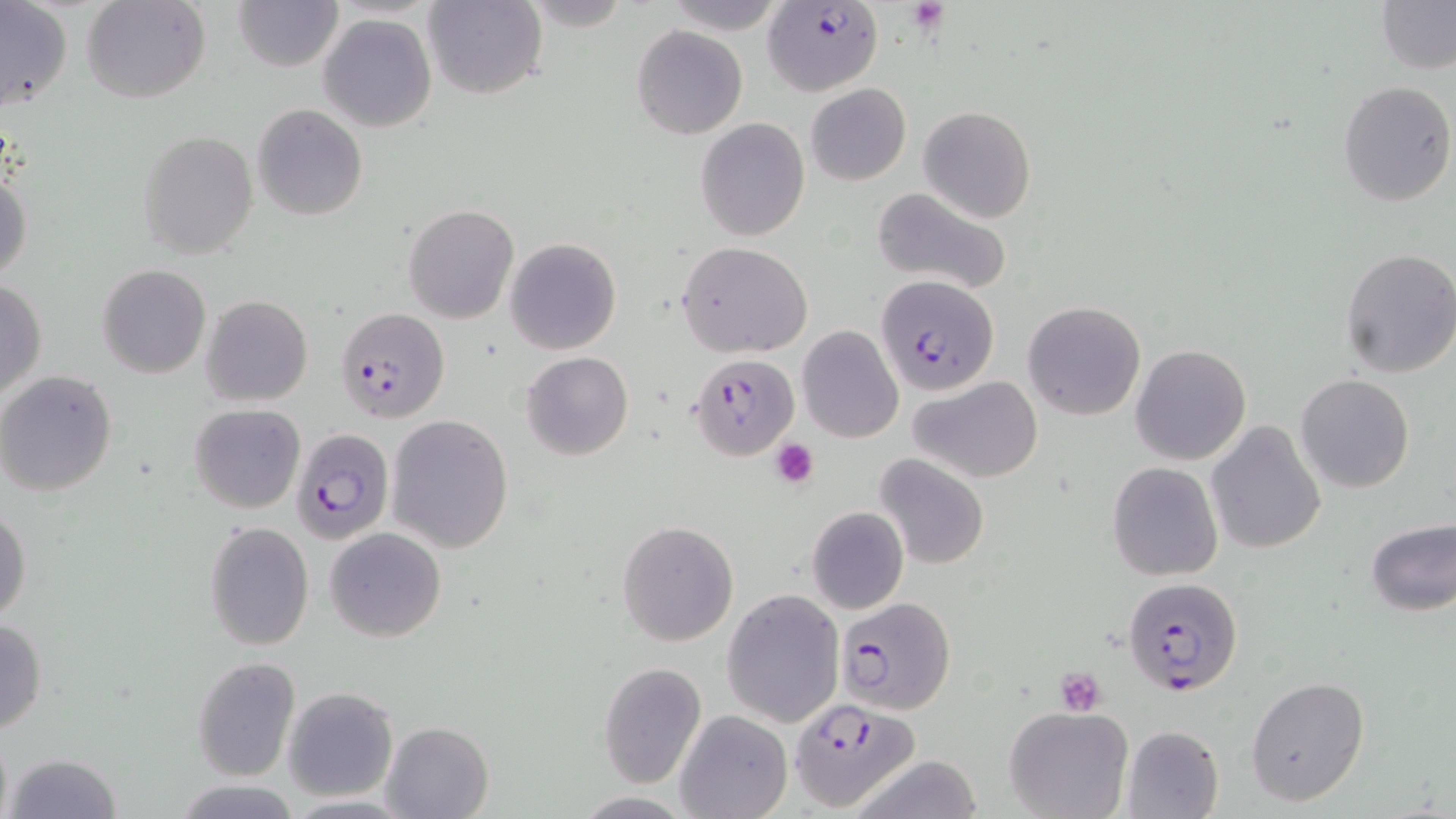
slide-level diagnosis = Plasmodium falciparum
platelet locations = approximate bounding boxes as [x1, y1, x2, y2] in pixels: [908, 0, 950, 34], [769, 438, 819, 487], [1054, 667, 1107, 715]
uninfected red blood cell locations (subset) = approximate bounding boxes as [x1, y1, x2, y2] in pixels: [83, 0, 210, 105], [233, 0, 344, 72], [424, 0, 545, 100], [661, 0, 788, 32], [1376, 1, 1456, 75], [0, 3, 72, 111], [319, 13, 436, 132], [631, 25, 747, 140], [1337, 80, 1455, 207], [805, 83, 911, 186], [251, 103, 369, 221], [918, 106, 1037, 222], [694, 117, 810, 241], [138, 129, 258, 258], [0, 171, 32, 284], [868, 187, 1014, 296], [403, 204, 520, 325], [504, 238, 622, 355], [677, 241, 813, 358], [1338, 246, 1456, 378], [97, 265, 212, 380], [0, 281, 47, 403], [202, 295, 313, 406], [1021, 301, 1146, 421], [796, 326, 904, 443], [1130, 344, 1252, 466], [521, 351, 633, 461], [0, 371, 119, 498], [1295, 374, 1415, 493], [909, 376, 1042, 482], [189, 403, 304, 514], [386, 415, 514, 553], [1206, 421, 1326, 555], [876, 453, 989, 569], [1107, 461, 1223, 582], [1, 505, 32, 626], [807, 506, 909, 614], [1364, 517, 1456, 618], [616, 520, 740, 647], [204, 521, 314, 649], [325, 528, 446, 642], [723, 590, 846, 727], [0, 617, 48, 736], [191, 656, 300, 782], [596, 662, 707, 788], [1246, 676, 1370, 807], [283, 687, 398, 802], [1003, 703, 1133, 819], [676, 710, 793, 819], [380, 720, 495, 819], [1121, 724, 1224, 819], [6, 752, 122, 818], [846, 756, 987, 819], [172, 780, 305, 817]
field of view = one of a larger specimen
modality = light microscopy
image size = 1456×819 pixels
preparation = thin blood smear
magnification = 1000x
stain = May-Grünwald-Giemsa
Plasmodium falciparum-infected red blood cell locations (subset) = approximate bounding boxes as [x1, y1, x2, y2] in pixels: [762, 2, 883, 96], [875, 275, 1001, 397], [690, 354, 799, 460], [291, 430, 394, 545], [1122, 575, 1243, 697], [836, 598, 955, 714], [790, 698, 918, 809]